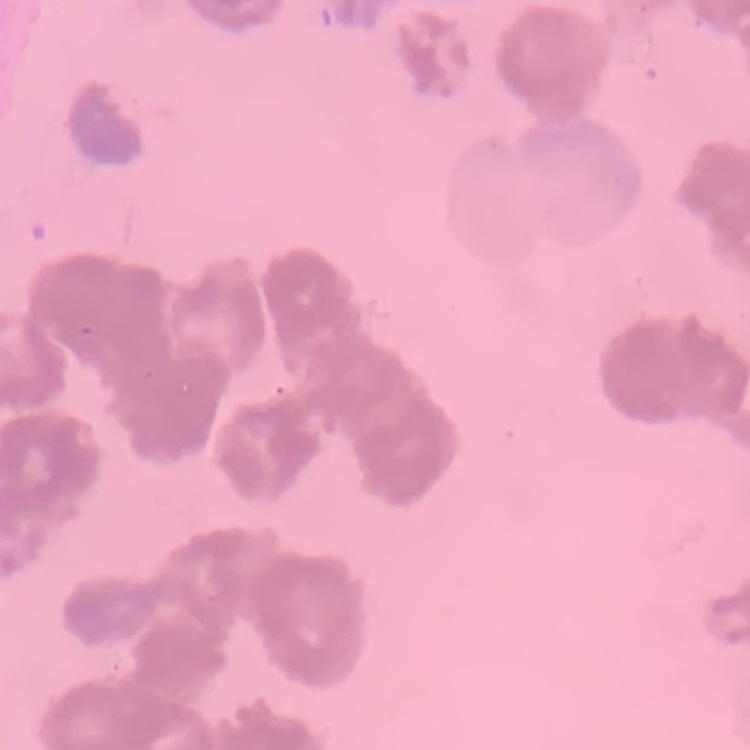
Summary:
  - Red blood cell morphology: rouleaux formation
  - Image type: one tile cut from a larger photomicrograph
  - Preparation: thin blood film
  - Stain: Field's or Giemsa